Comment on the morphology of the red blood cells.
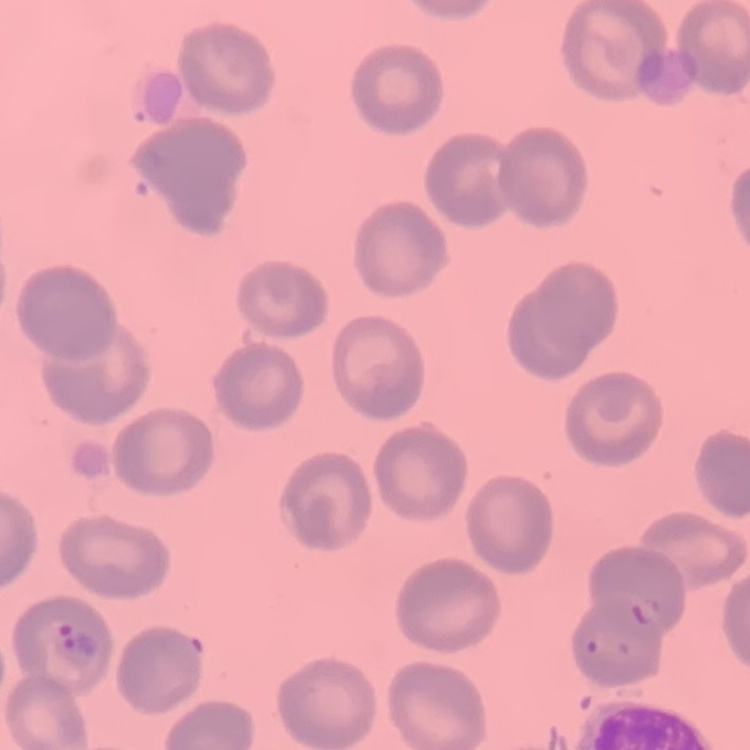
They show no rouleaux formation.

Summary:
  - Stain: Field's or Giemsa
  - Image type: square crop of a larger photomicrograph
  - Preparation: thin blood smear